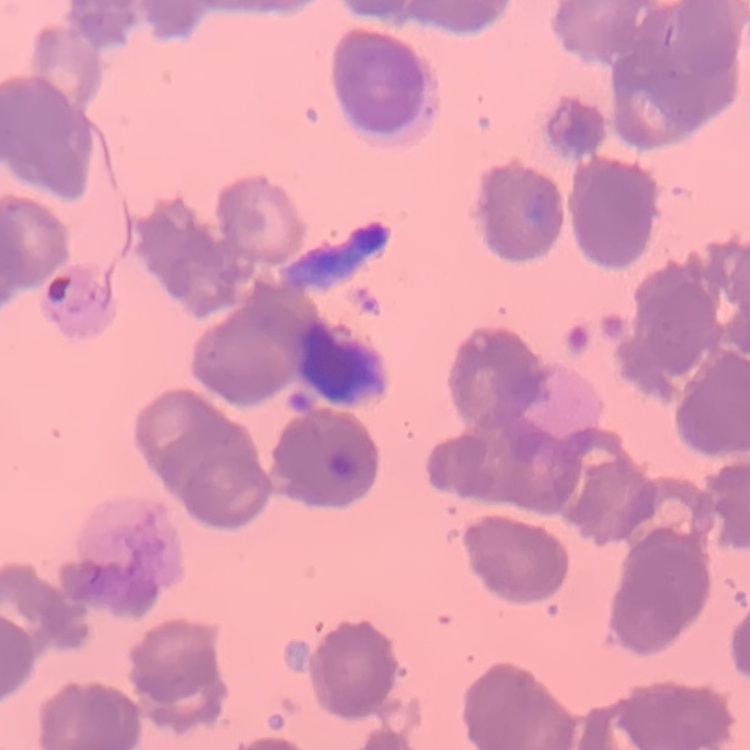

Summary:
  - Red blood cell morphology: rouleaux formation
  - Image type: one tile cut from a larger photomicrograph
  - Preparation: thin blood smear
  - Stain: Field's or Giemsa